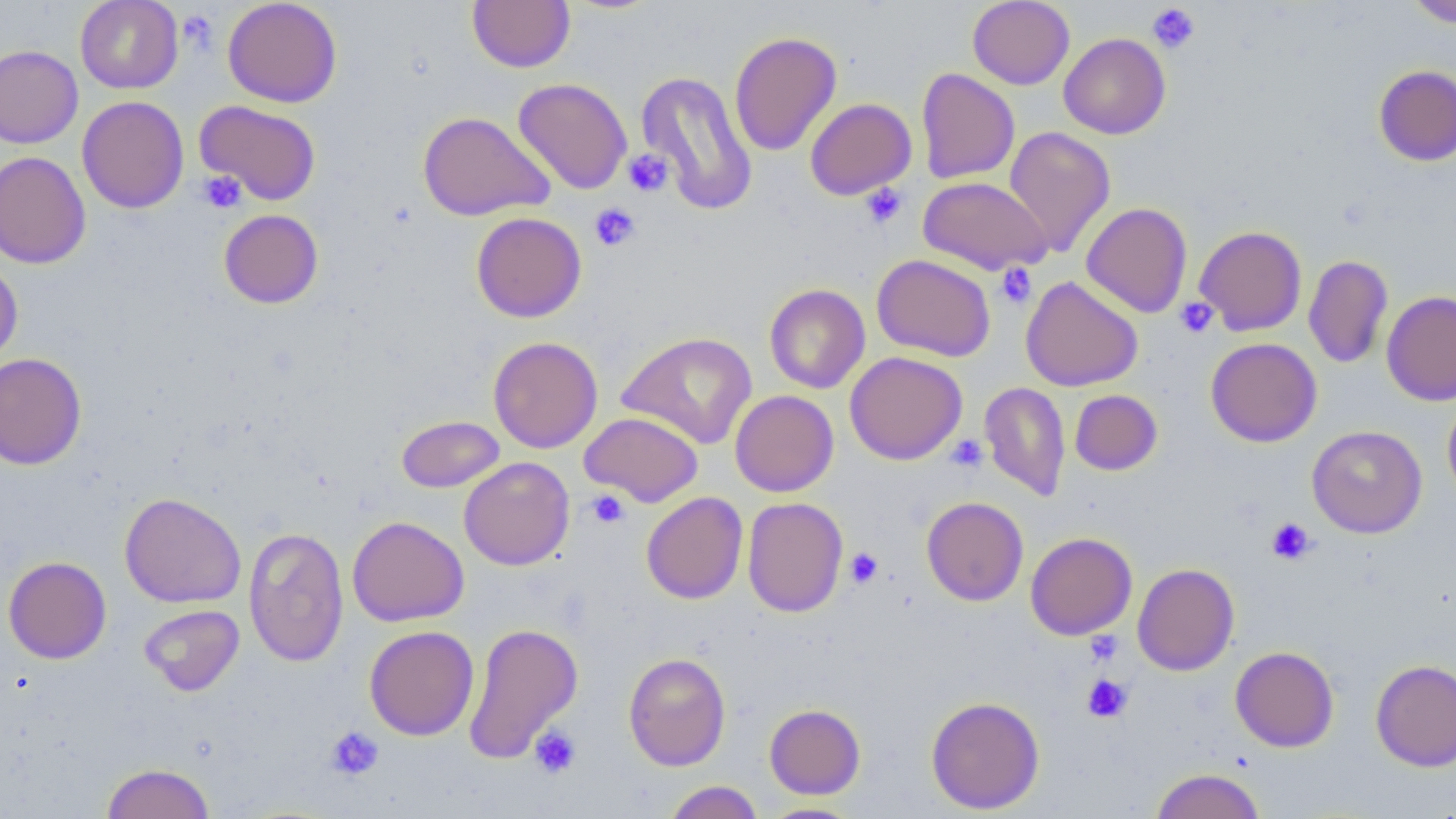
Approximate bounding boxes as (x1, y1, x2, y2) in pixels. Platelet locations: (1147, 3, 1201, 54), (177, 9, 219, 53), (623, 149, 673, 197), (196, 170, 247, 213), (860, 183, 908, 230), (589, 203, 641, 251), (995, 263, 1037, 308), (1174, 297, 1219, 338), (945, 435, 988, 473), (586, 490, 630, 529), (1266, 518, 1316, 564), (844, 547, 883, 589), (1085, 631, 1123, 667), (1082, 674, 1133, 723), (324, 725, 384, 781), (529, 725, 581, 779). Uninfected red blood cell locations: (75, 0, 184, 93), (222, 0, 343, 108), (467, 0, 575, 73), (967, 0, 1075, 89), (1404, 0, 1456, 28), (729, 31, 842, 156), (1059, 32, 1171, 139), (0, 44, 83, 148), (1374, 65, 1456, 167), (916, 67, 1020, 184), (637, 70, 758, 216), (513, 78, 633, 194), (76, 96, 189, 213), (805, 98, 917, 199), (194, 100, 321, 205), (418, 111, 553, 221), (1003, 126, 1116, 258), (0, 150, 91, 269), (917, 176, 1052, 274), (1081, 202, 1193, 318), (218, 209, 324, 309), (471, 212, 587, 322), (1194, 225, 1307, 335), (871, 254, 996, 362), (1303, 255, 1393, 368), (0, 259, 23, 368), (1020, 276, 1143, 391), (764, 284, 870, 394), (1381, 290, 1456, 406), (617, 331, 757, 449), (487, 336, 603, 453), (1205, 338, 1322, 447), (845, 351, 967, 465), (0, 352, 87, 470), (979, 382, 1071, 501), (1069, 389, 1163, 475), (730, 390, 838, 496), (1442, 398, 1456, 506), (579, 411, 703, 506), (397, 414, 504, 492), (1307, 425, 1427, 538), (459, 457, 575, 571), (119, 492, 246, 608), (641, 492, 748, 604), (921, 496, 1029, 606), (742, 497, 848, 617), (346, 516, 469, 626), (243, 525, 349, 668), (1025, 532, 1137, 640), (3, 556, 112, 664), (1132, 563, 1240, 676), (139, 604, 244, 696), (463, 622, 582, 764), (363, 625, 479, 740), (1230, 646, 1339, 752), (623, 652, 731, 771), (1370, 659, 1456, 772), (926, 695, 1045, 814), (764, 704, 866, 798), (101, 762, 216, 819), (1149, 768, 1266, 819), (663, 781, 764, 819), (758, 802, 866, 818). Slide-level diagnosis: negative for blood parasites. Optical microscopy. Single field of view. Captured at 1000x magnification. Thin blood smear. May-Grünwald-Giemsa stain. Image is 1456×819 pixels.